Name the parasite shown.
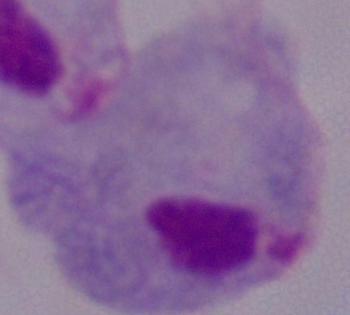

A trichomonad.

magnification = 1000x
modality = photomicrograph